Outline platelets.
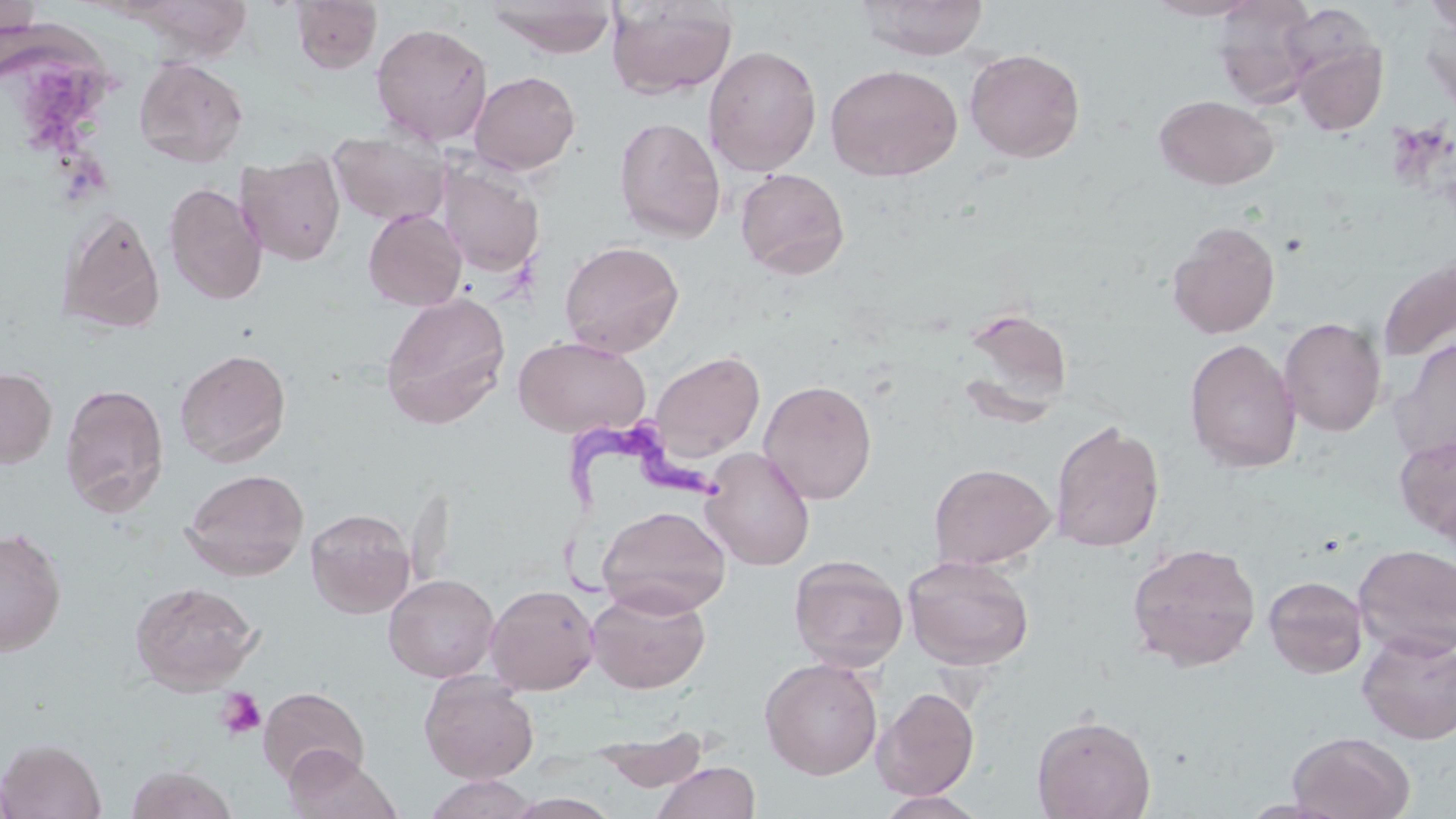
Approximate bounding boxes as [x1, y1, x2, y2] in pixels.
Platelets: [215, 687, 266, 738].

Summary:
  - Uninfected red blood cell locations: [290, 0, 382, 74], [485, 0, 619, 58], [858, 0, 990, 60], [1143, 0, 1265, 21], [1213, 0, 1319, 107], [1424, 0, 1456, 32], [606, 1, 738, 100], [1420, 12, 1456, 118], [370, 22, 494, 147], [1288, 31, 1388, 136], [703, 44, 822, 177], [964, 48, 1086, 162], [134, 56, 248, 167], [824, 63, 962, 181], [468, 70, 581, 176], [1153, 94, 1280, 190], [614, 116, 726, 243], [329, 130, 451, 227], [237, 152, 346, 266], [437, 161, 546, 278], [734, 167, 850, 279], [163, 183, 268, 305], [363, 208, 466, 311], [58, 209, 166, 335], [1167, 221, 1280, 340], [559, 240, 684, 358], [1377, 255, 1456, 363], [380, 291, 512, 428], [960, 308, 1074, 416], [1278, 316, 1387, 437], [513, 335, 650, 438], [1390, 337, 1456, 465], [1184, 338, 1302, 474], [174, 348, 291, 466], [649, 349, 765, 464], [0, 367, 57, 468], [758, 379, 877, 505], [59, 382, 170, 516], [1050, 419, 1165, 552], [1394, 433, 1456, 543], [700, 446, 816, 570], [929, 462, 1056, 570], [182, 468, 309, 580], [597, 504, 732, 617], [305, 507, 415, 618], [0, 527, 67, 656], [1126, 542, 1262, 671], [1353, 543, 1456, 659], [902, 554, 1035, 670], [788, 555, 909, 672], [384, 573, 499, 682], [1263, 575, 1369, 678], [129, 581, 260, 693], [484, 584, 599, 695], [585, 586, 711, 694], [1357, 630, 1456, 744], [759, 658, 883, 779], [419, 671, 540, 784], [258, 686, 368, 787], [872, 687, 980, 801], [1031, 714, 1156, 819], [593, 727, 710, 793], [1287, 731, 1415, 818], [0, 738, 106, 819], [285, 747, 401, 819], [652, 761, 761, 819], [125, 764, 237, 819], [423, 774, 538, 818], [875, 791, 988, 819], [503, 792, 622, 819]
  - Trypanosoma brucei locations: [558, 404, 729, 601]
  - Slide-level diagnosis: Trypanosoma brucei
  - Magnification: 1000x
  - Field of view: one of a larger specimen
  - Preparation: thin blood film
  - Image size: 1456×819 pixels
  - Stain: May-Grünwald-Giemsa
  - Modality: optical microscopy